Outline each blood parasite and name the species.
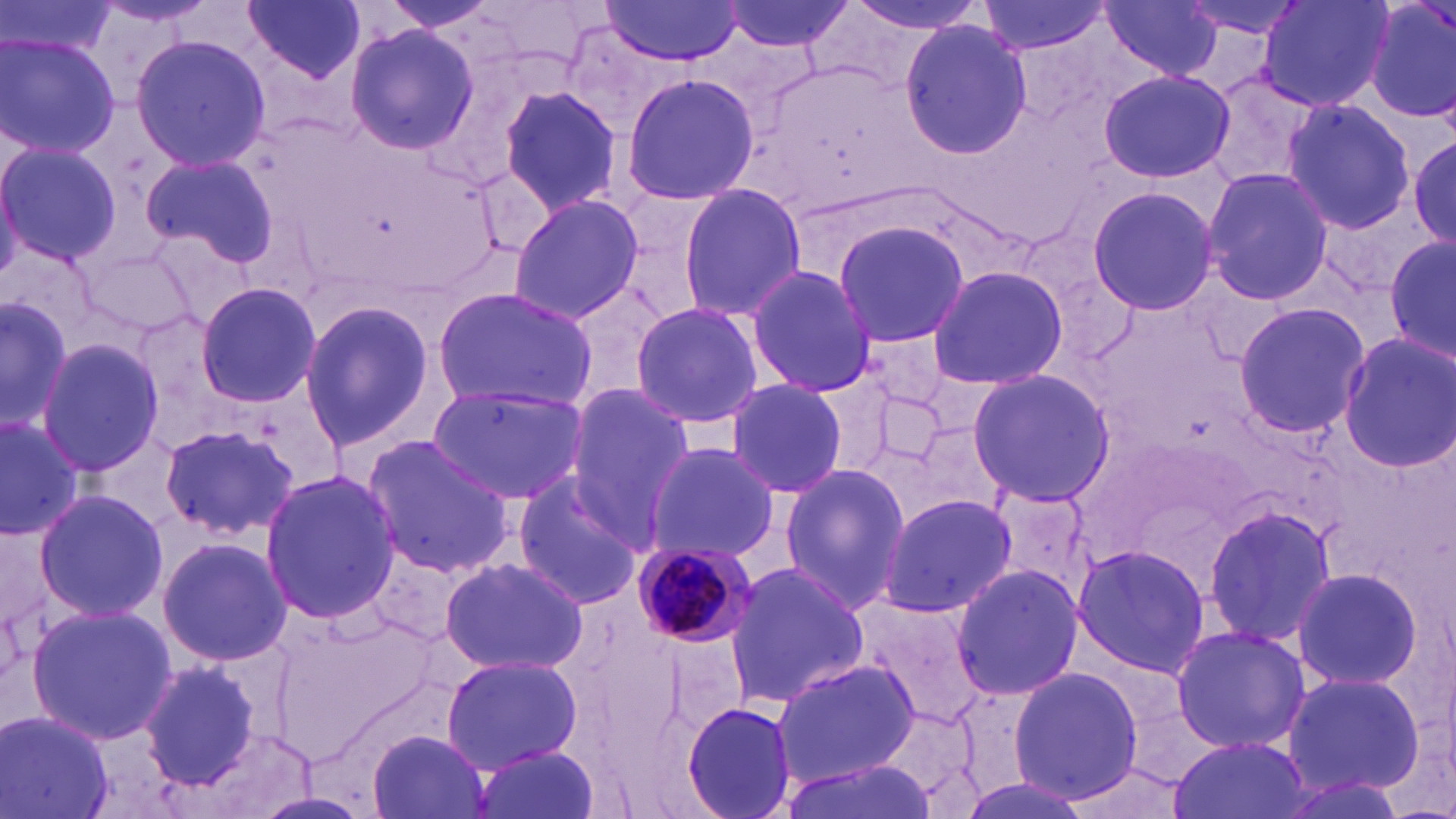
Approximate bounding boxes as [x1, y1, x2, y2] in pixels.
Plasmodium malariae-infected red blood cells: [626, 543, 754, 650].
No Plasmodium falciparum, Plasmodium ovale, Plasmodium vivax, Babesia divergens, or Trypanosoma brucei observed.

Uninfected red blood cell locations: [3, 0, 119, 60], [242, 0, 368, 83], [597, 0, 745, 64], [716, 0, 852, 55], [977, 0, 1112, 56], [1097, 0, 1226, 84], [1256, 0, 1392, 113], [1364, 0, 1455, 128], [377, 1, 503, 35], [845, 1, 991, 35], [1177, 3, 1312, 41], [899, 18, 1033, 157], [343, 22, 479, 156], [0, 33, 119, 160], [130, 35, 270, 171], [1200, 68, 1322, 191], [1098, 69, 1237, 185], [622, 74, 759, 206], [496, 85, 623, 213], [1281, 98, 1417, 235], [1409, 134, 1456, 248], [0, 140, 121, 268], [141, 149, 277, 268], [1201, 167, 1334, 306], [677, 183, 808, 321], [1085, 185, 1219, 316], [509, 195, 644, 321], [828, 221, 970, 350], [1385, 236, 1456, 363], [3, 244, 100, 346], [744, 265, 878, 395], [926, 265, 1068, 390], [194, 280, 322, 408], [432, 288, 596, 411], [0, 292, 73, 436], [297, 298, 437, 455], [629, 301, 765, 428], [1231, 302, 1370, 437], [132, 307, 237, 428], [1337, 333, 1456, 471], [36, 338, 166, 478], [965, 369, 1117, 506], [725, 377, 847, 497], [426, 382, 588, 502], [561, 384, 694, 533], [862, 387, 954, 471], [0, 414, 83, 535], [901, 419, 1009, 527], [157, 423, 300, 539], [361, 436, 517, 575], [644, 442, 778, 561], [778, 463, 911, 612], [259, 468, 403, 629], [509, 473, 644, 608], [31, 489, 168, 623], [878, 493, 1018, 616], [1200, 502, 1337, 651], [156, 535, 295, 667], [1068, 542, 1212, 679], [439, 556, 589, 676], [725, 561, 870, 708], [948, 563, 1084, 703], [1290, 565, 1425, 692], [850, 595, 988, 724], [26, 603, 177, 746], [275, 611, 445, 762], [1170, 626, 1313, 754], [440, 654, 586, 772], [138, 657, 268, 792], [770, 658, 920, 786], [1008, 665, 1143, 804], [1281, 668, 1426, 796], [679, 701, 799, 818], [0, 708, 116, 819], [367, 729, 492, 819], [1168, 734, 1313, 819], [465, 745, 603, 819], [777, 755, 938, 819]. Slide-level diagnosis: Plasmodium malariae. Light microscopy. May-Grünwald-Giemsa stain. 1000x magnification. Image is 1456×819 pixels. Thin blood film. One field of a larger specimen.